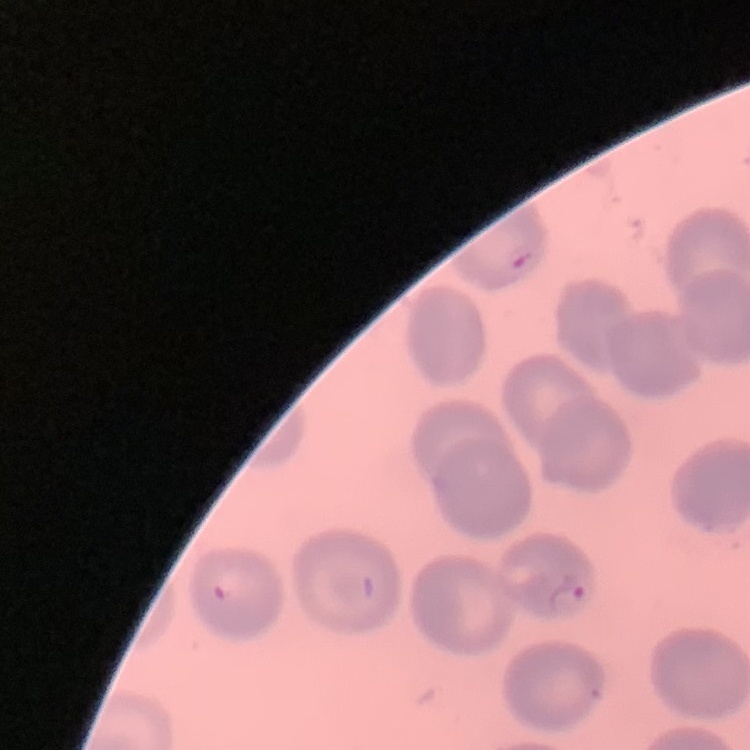

The red blood cells exhibit no rouleaux formation. Thin peripheral smear. One tile cut from a larger photomicrograph. Field's or Giemsa stain.